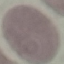
Summary:
  - Result: negative for malaria parasites
  - Preparation: thin blood smear
  - Stain: Giemsa
  - Capture: smartphone through the microscope eyepiece
  - Image type: cell patch, automatically extracted from a larger field of view and resized to 64 × 64 pixels